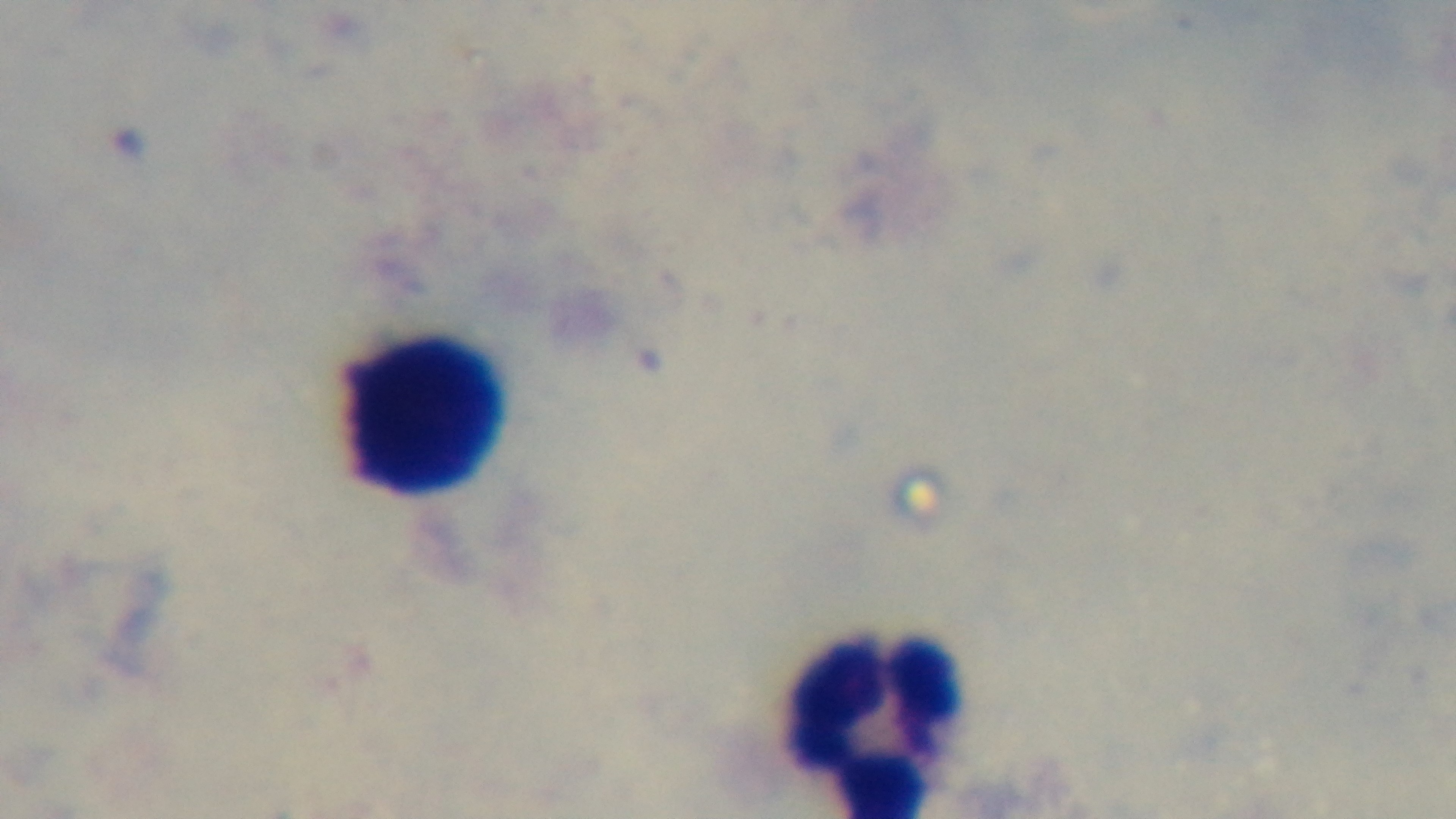
objective: 100x oil immersion
malaria_status: uninfected
preparation: thick blood film
field_of_view: single
stain: Giemsa
capture: mounted 4K digital camera
modality: light microscopy